Assess this cell for malaria.
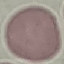

Uninfected.

image type = automatically extracted cell patch, resized to 64 × 64 pixels
preparation = thin blood film
stain = Giemsa
capture = smartphone through the microscope eyepiece